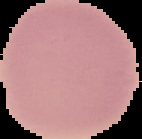
Result: negative for Plasmodium parasites. Segmented cell region on a black background. Image is 142×139 pixels. From a thin blood smear.